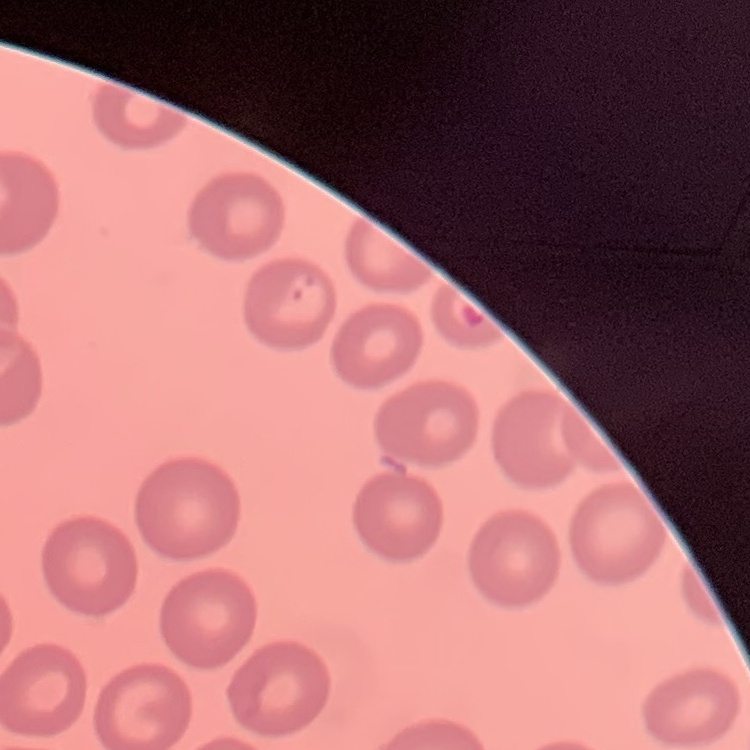

Summary:
  - Erythrocyte morphology: no rouleaux formation
  - Image type: square crop of a larger photomicrograph
  - Preparation: thin peripheral smear
  - Stain: Field's or Giemsa